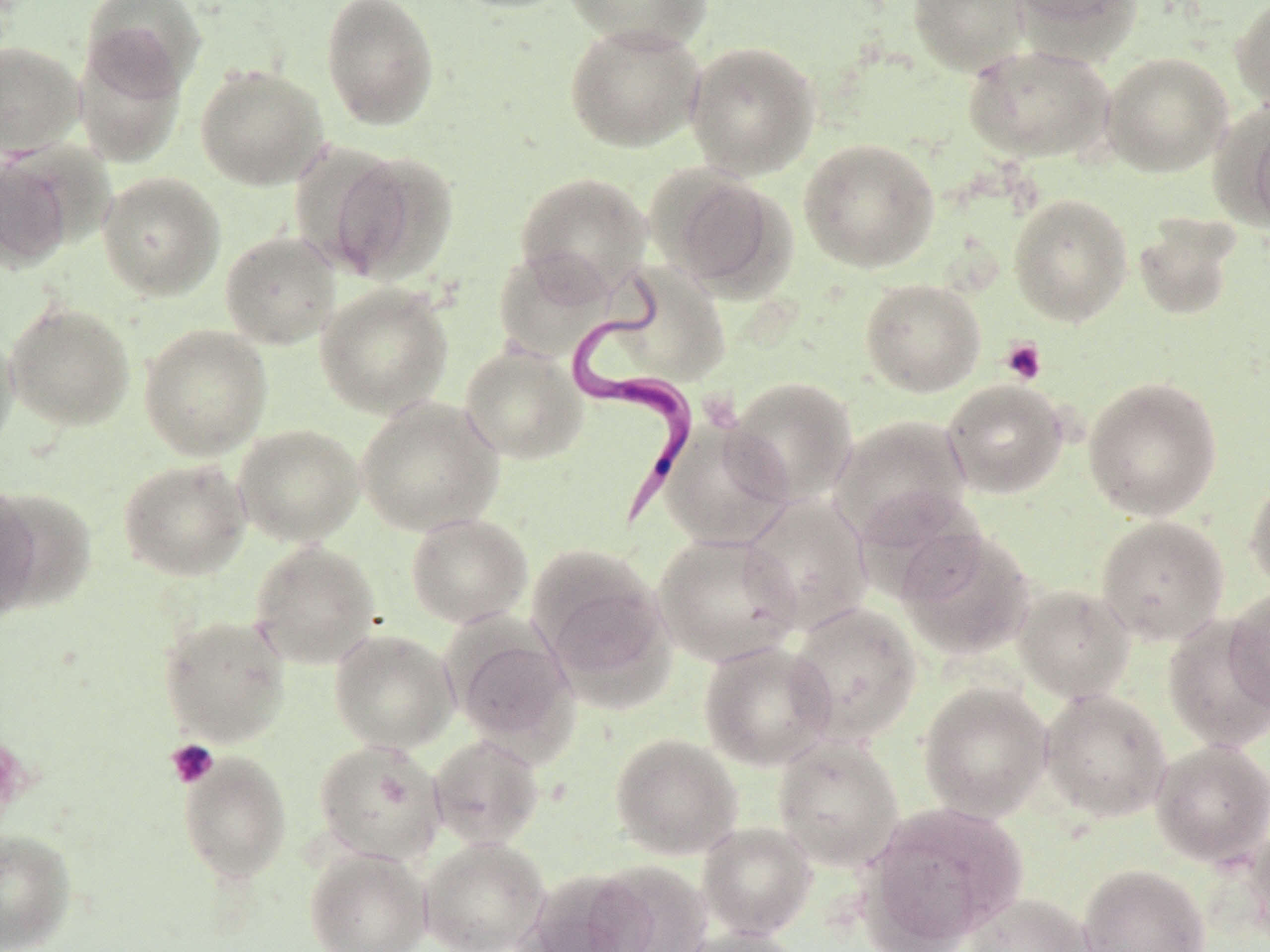

Summary:
  - Coordinate format: approximate bounding boxes as (x1, y1, x2, y2) in pixels
  - Uninfected red blood cell locations: (320, 0, 440, 131), (444, 0, 577, 14), (562, 0, 714, 51), (908, 0, 1030, 76), (1010, 0, 1139, 35), (1231, 0, 1270, 112), (81, 1, 206, 101), (564, 23, 705, 152), (72, 36, 187, 168), (685, 40, 821, 179), (0, 41, 85, 159), (963, 44, 1115, 164), (1101, 51, 1233, 177), (195, 64, 330, 190), (1229, 103, 1270, 231), (287, 139, 410, 279), (799, 139, 940, 273), (327, 149, 459, 284), (0, 154, 74, 272), (657, 170, 793, 296), (98, 171, 226, 300), (514, 171, 653, 298), (1008, 193, 1133, 326), (1133, 217, 1240, 321), (220, 230, 342, 349), (493, 247, 615, 364), (613, 264, 732, 386), (860, 278, 986, 397), (315, 283, 453, 419), (5, 301, 136, 430), (138, 324, 273, 460), (0, 328, 19, 459), (460, 344, 587, 464), (727, 376, 858, 505), (1082, 376, 1222, 521), (942, 379, 1068, 498), (356, 396, 504, 537), (830, 415, 974, 545), (659, 418, 794, 550), (233, 424, 365, 546), (118, 458, 251, 581), (1245, 475, 1270, 594), (0, 485, 42, 618), (1, 487, 94, 613), (740, 496, 873, 634), (406, 512, 532, 628), (1095, 515, 1230, 645), (898, 529, 1036, 661), (652, 533, 801, 667), (249, 541, 381, 669), (528, 544, 671, 690), (1013, 584, 1136, 703), (1225, 587, 1270, 716), (787, 600, 922, 745), (158, 614, 291, 746), (1161, 616, 1269, 752), (329, 628, 459, 753), (451, 630, 578, 753), (699, 640, 836, 770), (917, 681, 1053, 821), (1039, 688, 1173, 823), (428, 733, 545, 849), (610, 733, 742, 860), (772, 736, 904, 871), (314, 739, 446, 865), (1150, 739, 1270, 867), (178, 751, 292, 882), (859, 803, 1025, 950), (697, 821, 817, 939), (1243, 824, 1270, 949), (0, 828, 77, 952), (419, 836, 550, 952), (304, 846, 432, 952), (589, 861, 714, 952), (1077, 863, 1210, 952), (520, 868, 656, 952), (963, 893, 1093, 952), (674, 926, 806, 952)
  - Platelet locations: (1000, 337, 1047, 385), (166, 739, 220, 789)
  - Trypanosoma brucei locations: (563, 271, 700, 527)
  - Slide-level diagnosis: Trypanosoma brucei
  - Magnification: 1000x
  - Modality: light microscopy
  - Field of view: one of a larger specimen
  - Stain: May-Grünwald-Giemsa
  - Preparation: thin blood film
  - Image size: 1270×952 pixels